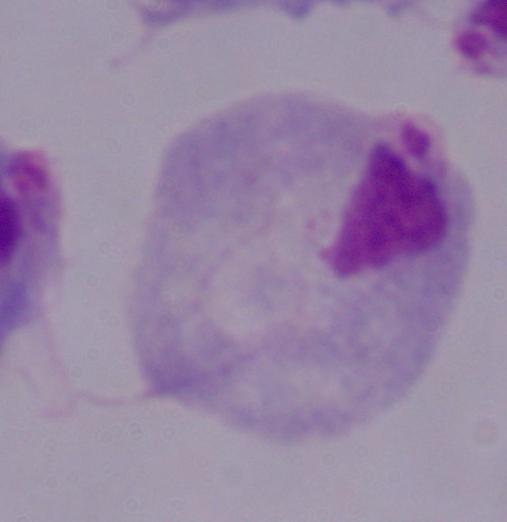

A trichomonad is shown. Photomicrograph. 1000x magnification.